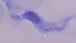

Summary:
  - Identification: trypanosome
  - Modality: photomicrograph
  - Magnification: 1000x